Evaluate for parasitized red blood cells.
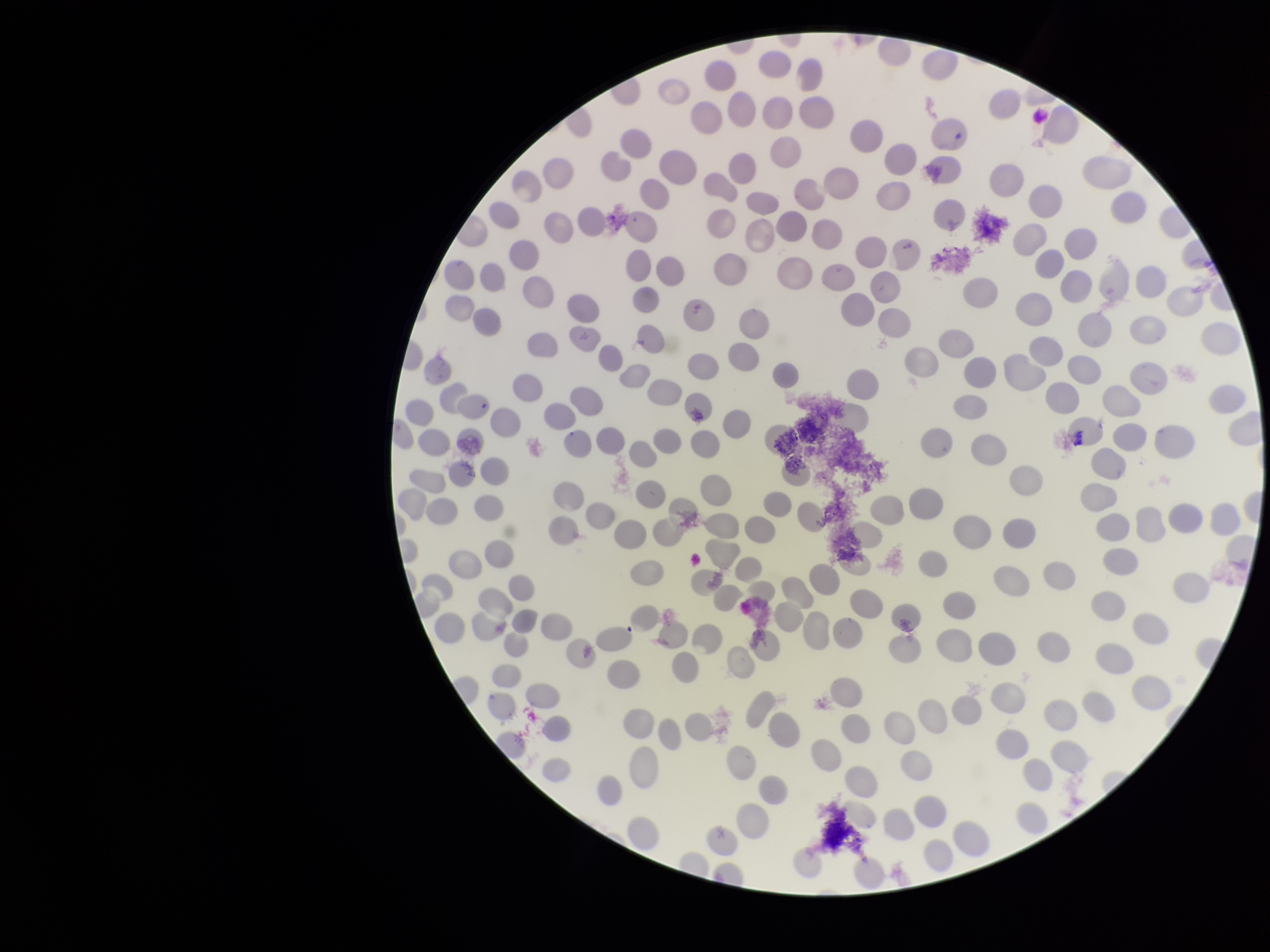
None identified.

{
  "preparation": "thin",
  "parasitized_red_blood_cell_count": 0,
  "field_of_view": "one from this slide",
  "image_size": "1270×952 pixels",
  "patient_malaria_status": "negative",
  "stain": "Giemsa",
  "red_blood_cell_count": 228,
  "capture": "smartphone photograph through the microscope eyepiece"
}